Name the blood parasite species.
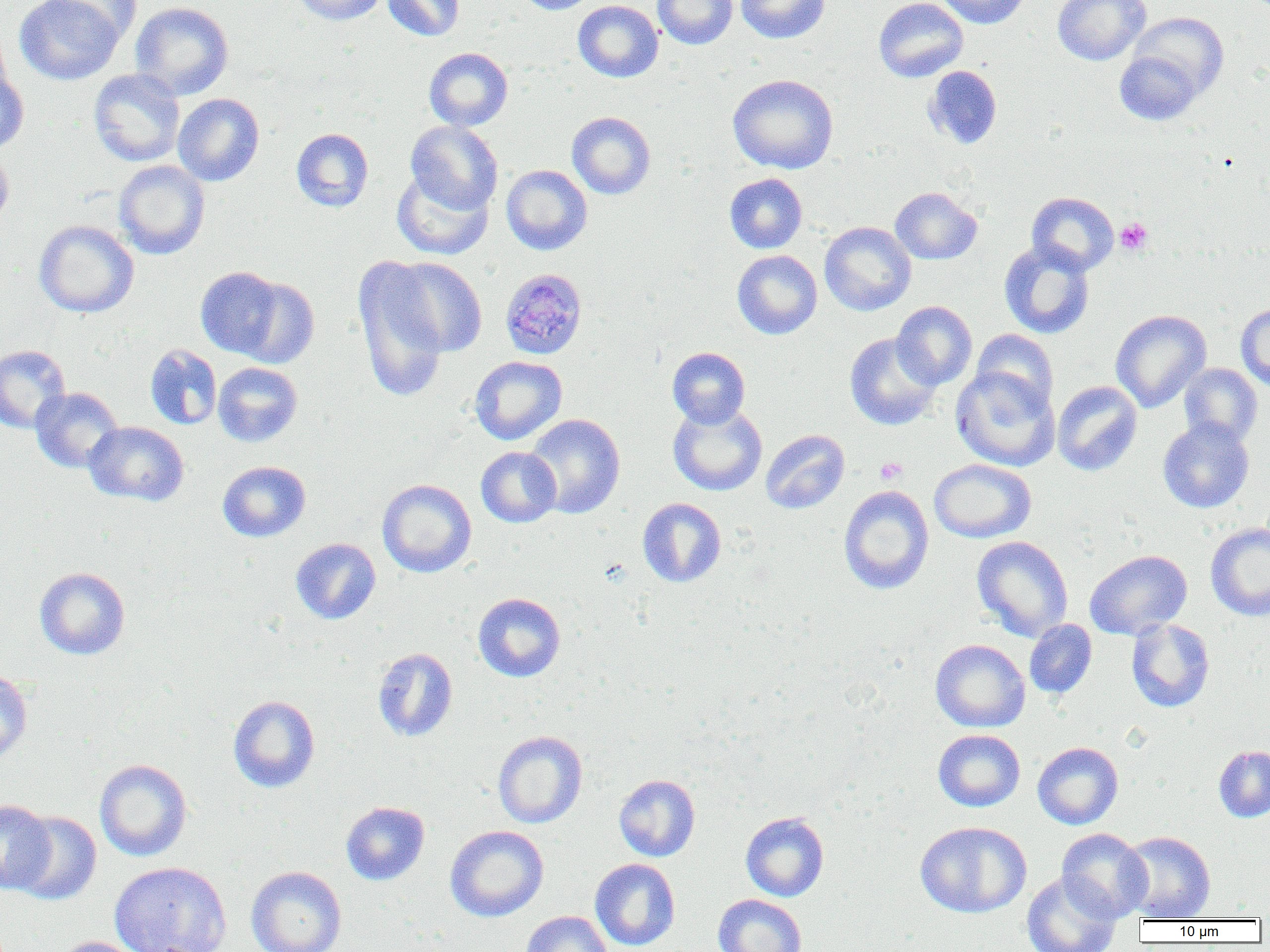
Plasmodium malariae.

Summary:
  - Coordinate format: approximate bounding boxes as [x1, y1, x2, y2] in pixels
  - Plasmodium malariae-infected red blood cell locations: [499, 268, 587, 360]
  - Platelet locations: [1115, 218, 1152, 254], [875, 457, 907, 484]
  - Uninfected red blood cell locations: [14, 0, 124, 85], [49, 0, 142, 45], [291, 0, 387, 25], [382, 0, 465, 41], [514, 0, 599, 14], [573, 0, 663, 82], [652, 0, 738, 49], [735, 0, 830, 44], [873, 0, 968, 82], [935, 0, 1031, 28], [1053, 0, 1150, 65], [130, 1, 234, 100], [1128, 12, 1229, 100], [0, 24, 13, 108], [424, 47, 513, 131], [1114, 50, 1203, 126], [924, 65, 1002, 149], [0, 69, 29, 155], [88, 69, 185, 167], [728, 74, 839, 174], [173, 93, 264, 186], [567, 111, 656, 199], [405, 121, 503, 214], [291, 128, 374, 212], [0, 145, 14, 231], [113, 160, 210, 260], [501, 165, 593, 255], [392, 169, 493, 260], [724, 173, 807, 253], [890, 187, 982, 264], [1027, 192, 1119, 275], [34, 220, 139, 318], [819, 222, 916, 316], [999, 241, 1095, 339], [732, 250, 822, 339], [386, 257, 487, 358], [353, 258, 451, 404], [195, 266, 284, 359], [234, 276, 320, 369], [892, 301, 977, 389], [1235, 303, 1270, 391], [1110, 309, 1211, 412], [970, 328, 1059, 413], [844, 333, 942, 430], [0, 344, 71, 434], [144, 344, 222, 430], [667, 347, 750, 428], [469, 356, 567, 445], [213, 362, 302, 447], [1178, 363, 1263, 447], [951, 367, 1060, 471], [1052, 381, 1142, 476], [31, 387, 123, 473], [668, 402, 767, 496], [524, 414, 625, 518], [1157, 418, 1254, 513], [83, 421, 189, 506], [761, 429, 849, 513], [476, 447, 562, 527], [929, 459, 1036, 543], [217, 461, 311, 542], [377, 478, 477, 578], [838, 485, 934, 595], [638, 498, 726, 587], [1205, 521, 1270, 621], [971, 536, 1073, 642], [290, 538, 381, 624], [1085, 549, 1192, 640], [34, 567, 130, 659], [472, 592, 566, 682], [1024, 619, 1097, 699], [1126, 619, 1215, 712], [930, 639, 1030, 732], [372, 647, 458, 742], [0, 667, 33, 766], [228, 695, 320, 792], [933, 729, 1025, 812], [493, 730, 588, 828], [1033, 741, 1123, 830], [1213, 745, 1270, 822], [94, 759, 192, 861], [613, 774, 700, 862], [0, 799, 55, 894], [341, 801, 430, 885], [9, 810, 102, 905], [740, 812, 829, 901], [915, 821, 1031, 918], [445, 825, 549, 922], [1056, 828, 1152, 921], [1118, 831, 1216, 921], [590, 858, 680, 950], [109, 860, 232, 952], [246, 865, 347, 952], [1021, 871, 1122, 952], [713, 894, 807, 952], [521, 911, 614, 952], [54, 936, 147, 952]
  - Modality: optical microscopy
  - Field of view: one of a larger specimen
  - Image size: 1270×952 pixels
  - Magnification: 1000x
  - Preparation: thin blood film